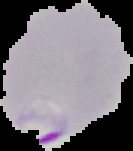

From a thin blood smear. The area outside the segmented cell region is set to black. Malaria status: parasitized. Image is 133×151 pixels.